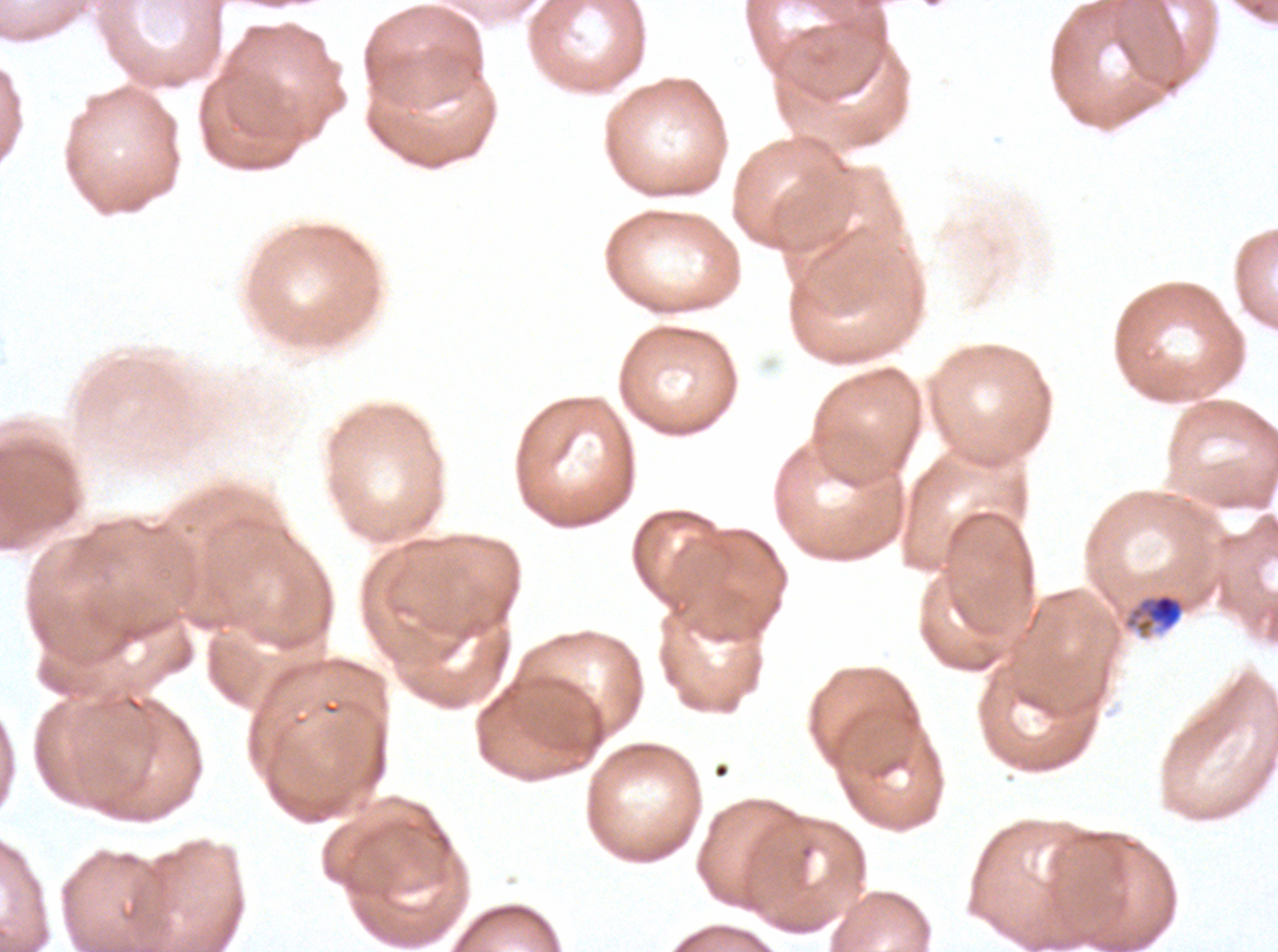

Approximate bounding boxes as [x1, y1, x2, y2] in pixels.
Summary:
  - Mid trophozoite locations: [1131, 592, 1184, 633]
  - Image size: 1278×952 pixels
  - Field of view: one sub-image of a larger composite
  - Stain: Giemsa
  - Preparation: thin blood smear
  - Specimen: Plasmodium falciparum cultured ex vivo for 24 to 48 hours, from a patient in The Gambia